Outline each Plasmodium ovale-infected red blood cell.
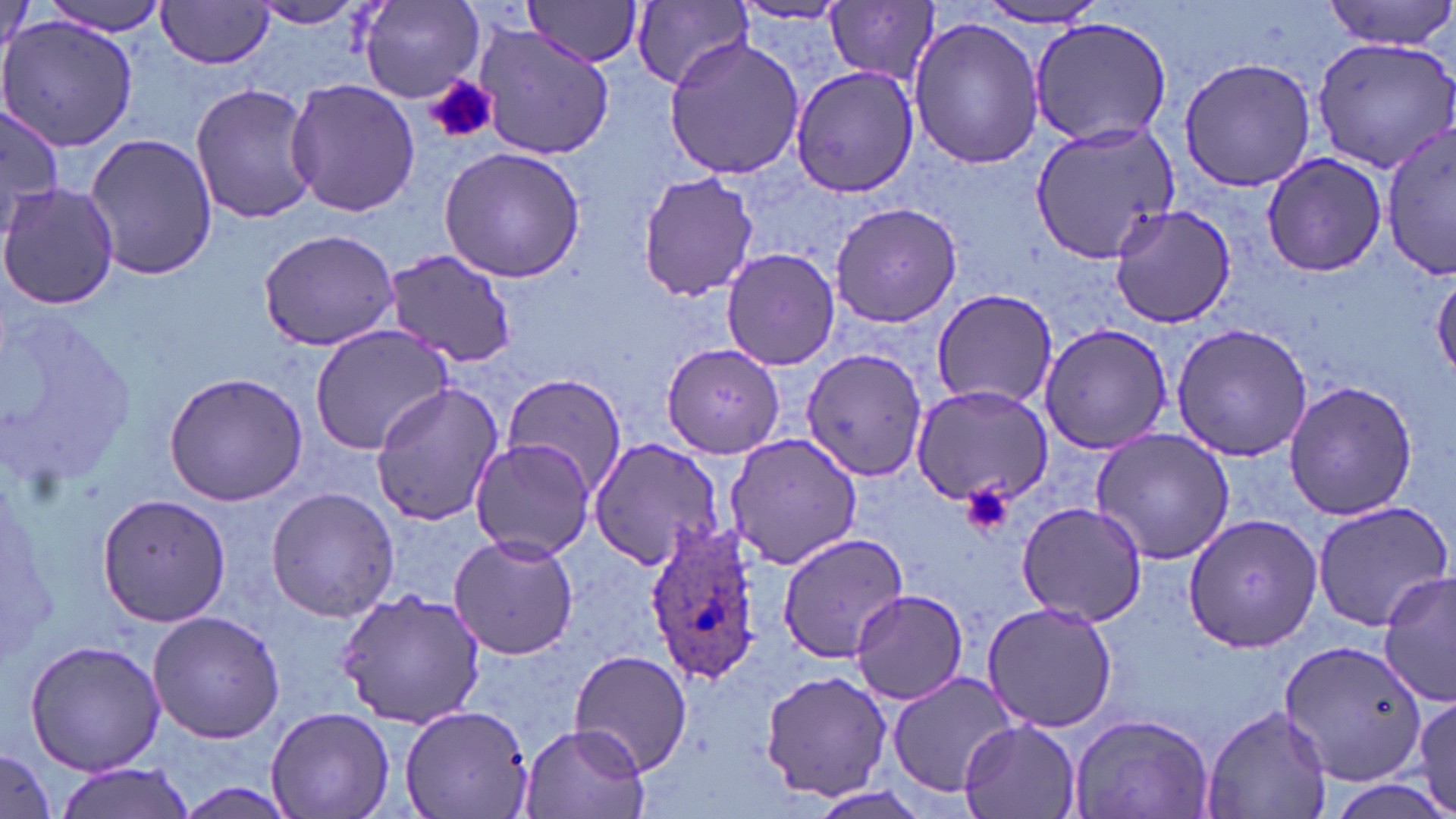

Approximate bounding boxes as (x1, y1, x2, y2) in pixels.
Plasmodium ovale-infected red blood cells: (642, 524, 766, 684).

slide_level_diagnosis: Plasmodium ovale
image_size: 1456×819 pixels
uninfected_red_blood_cell_locations: 'approximate bounding boxes as (x1, y1, x2, y2) in pixels: (34, 0, 168, 34), (1320, 0, 1456, 49), (359, 1, 487, 102), (522, 1, 644, 68), (628, 1, 754, 91), (249, 2, 367, 31), (825, 2, 940, 83), (156, 3, 276, 70), (971, 3, 1110, 29), (730, 4, 853, 27), (906, 14, 1046, 168), (1029, 16, 1174, 149), (0, 17, 137, 152), (474, 25, 614, 161), (1311, 34, 1456, 174), (663, 37, 809, 181), (1176, 55, 1317, 193), (788, 64, 920, 196), (286, 78, 419, 218), (191, 83, 318, 224), (2, 104, 63, 239), (1382, 120, 1455, 283), (1031, 122, 1181, 263), (82, 132, 220, 281), (438, 146, 587, 284), (1260, 152, 1387, 278), (637, 170, 759, 301), (1, 182, 118, 311), (828, 201, 962, 328), (1109, 203, 1239, 328), (258, 229, 401, 353), (720, 247, 842, 371), (381, 250, 518, 369), (1432, 273, 1456, 381), (930, 287, 1060, 409), (1037, 322, 1175, 454), (1171, 323, 1315, 462), (309, 325, 454, 455), (661, 343, 785, 460), (802, 349, 925, 480), (162, 372, 308, 506), (498, 374, 627, 495), (369, 381, 502, 526), (1283, 381, 1419, 520), (908, 384, 1055, 506), (1090, 426, 1235, 565), (723, 429, 861, 572), (468, 437, 595, 562), (589, 438, 730, 572), (265, 487, 401, 623), (96, 492, 232, 628), (1017, 499, 1148, 627), (1311, 500, 1452, 631), (1182, 511, 1323, 654), (776, 531, 912, 662), (448, 534, 581, 662), (1379, 571, 1455, 709), (332, 586, 488, 729), (848, 589, 969, 706), (980, 603, 1119, 734), (146, 609, 285, 743), (1277, 638, 1429, 789), (24, 640, 166, 775), (568, 650, 694, 774), (759, 670, 893, 800), (885, 670, 1025, 797), (1406, 684, 1456, 819), (399, 704, 533, 819), (1203, 704, 1333, 819), (264, 707, 395, 819), (1068, 711, 1215, 819), (959, 720, 1081, 819), (518, 722, 650, 819), (0, 745, 56, 819), (55, 762, 193, 819)'
modality: light microscopy
preparation: thin blood film
magnification: 1000x
field_of_view: one of a larger specimen
platelet_locations: 'approximate bounding boxes as (x1, y1, x2, y2) in pixels: (424, 76, 499, 145), (961, 483, 1014, 536)'
stain: May-Grünwald-Giemsa